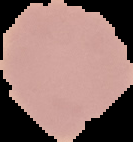
Summary:
  - Image size: 133×142 pixels
  - Preparation: thin blood smear
  - Result: no Plasmodium parasites seen
  - Image type: cell region segmented out of the field of view; surrounding area masked to black